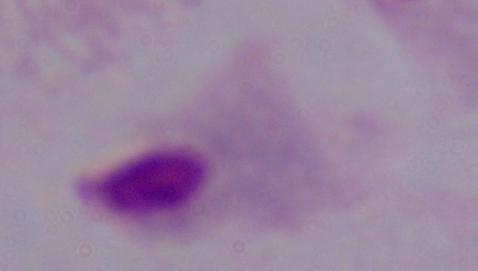
A trichomonad is seen. Micrograph. Captured at 1000x magnification.